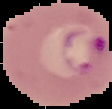

image size = 112×109 pixels
image type = segmented cell region with the area outside set to black
preparation = thin blood smear
malaria status = parasitized